Locate every Plasmodium parasite.
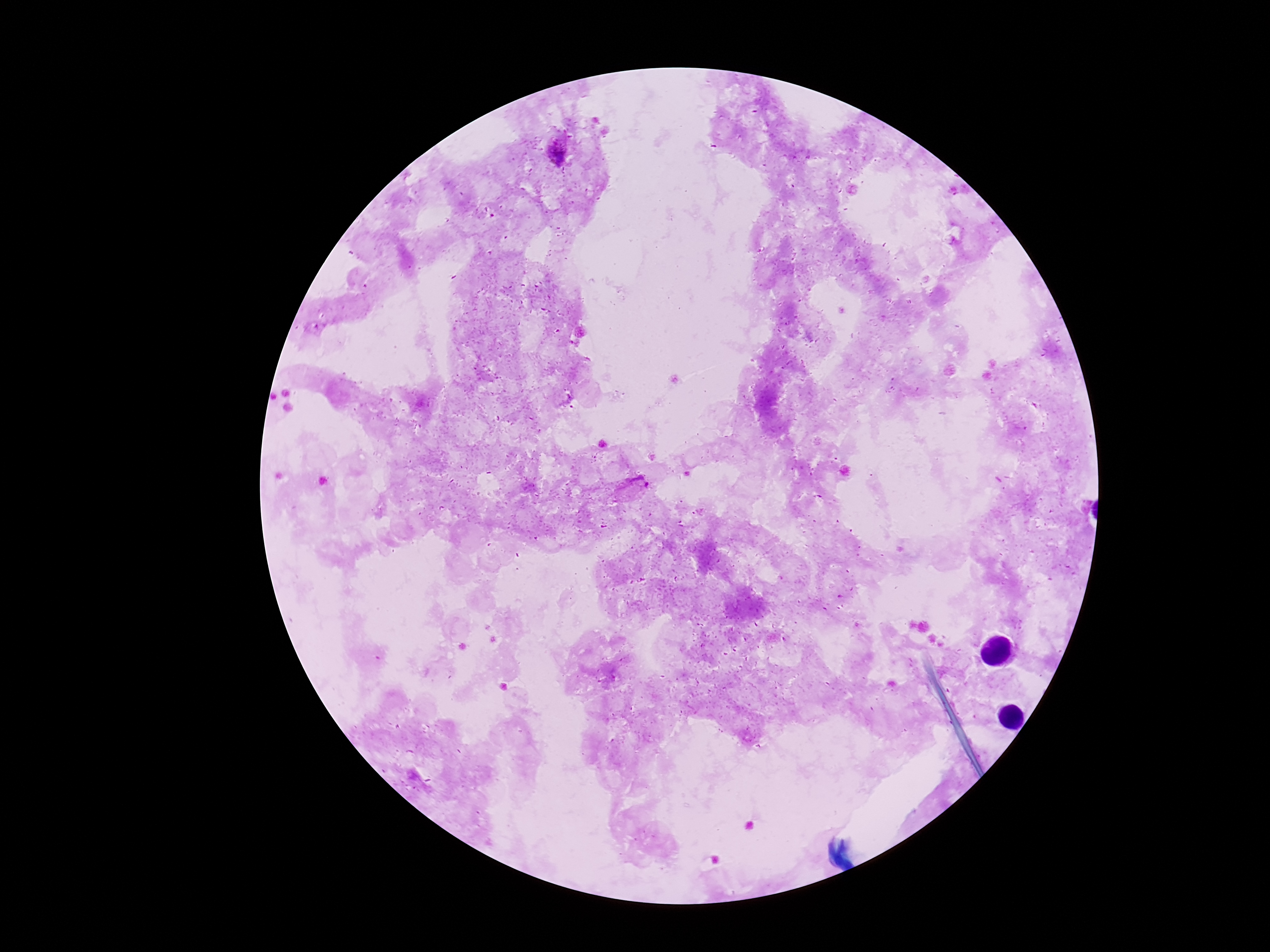
Approximate centers as [x, y] in pixels.
Plasmodium parasites: [555, 150], [633, 489].

preparation = thick blood film
capture = smartphone camera through the microscope eyepiece
magnification = 100x
patient malaria status = infected
stain = Giemsa
image size = 1270×952 pixels
field of view = single